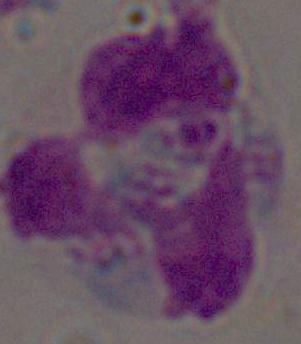

Summary:
  - Identification: leukocyte
  - Modality: micrograph
  - Magnification: 1000x